Classify this cell by malaria status.
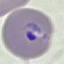

It is parasitized.

Summary:
  - Image type: automatically extracted cell patch, resized to 64 × 64 pixels
  - Preparation: thin blood smear
  - Stain: Giemsa
  - Capture: smartphone camera at the microscope eyepiece